Outline each blood parasite and name the species.
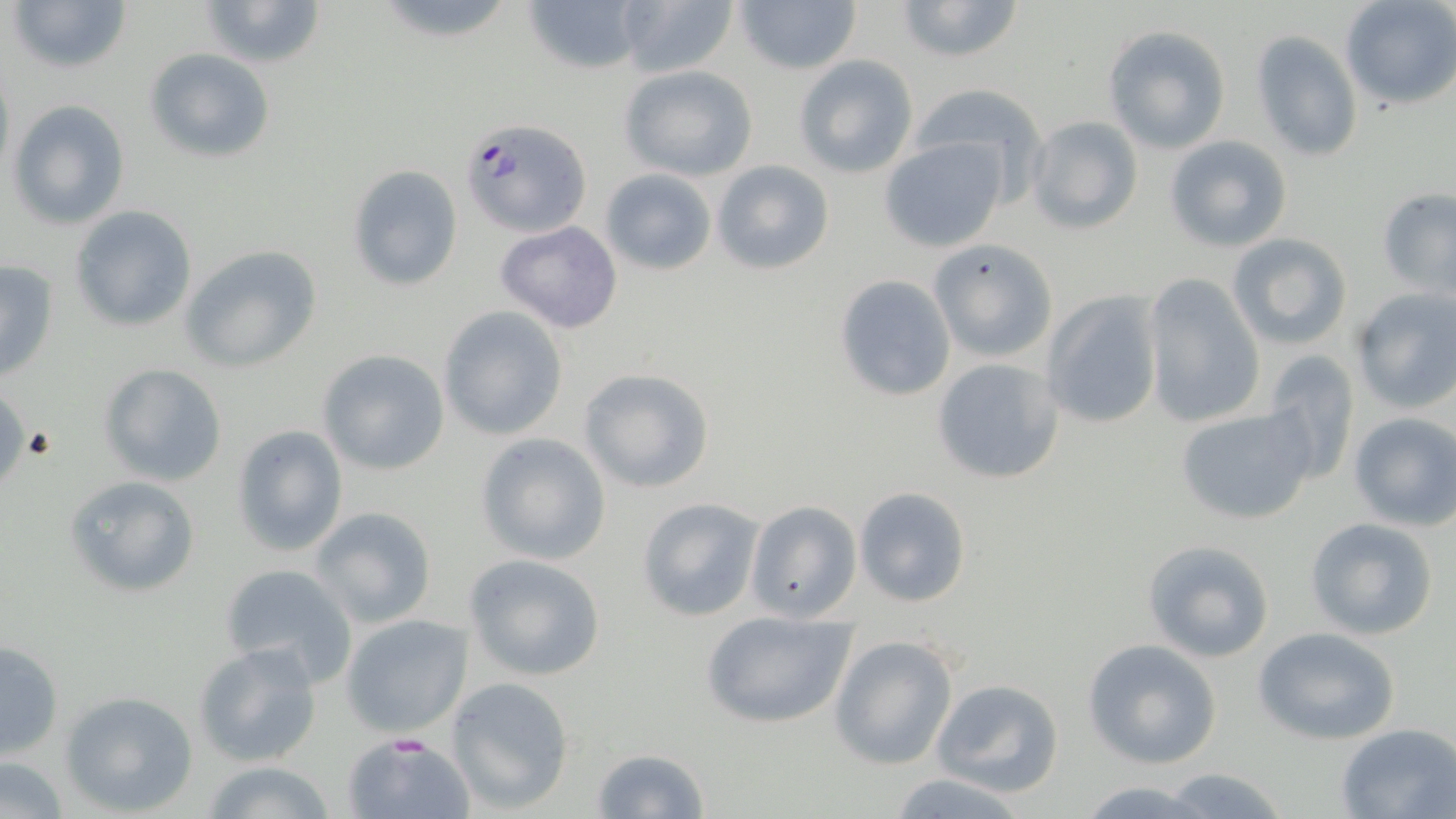

Approximate bounding boxes as (x1,y1)-(x2,y2) corner pairs in pixels.
Plasmodium falciparum-infected red blood cells: (460,120)-(590,238).
No Plasmodium ovale, Plasmodium malariae, Plasmodium vivax, Babesia divergens, or Trypanosoma brucei observed.

{
  "slide_level_diagnosis": "Plasmodium falciparum",
  "uninfected_red_blood_cell_locations": "approximate bounding boxes as (x1,y1)-(x2,y2) corner pairs in pixels: (7,0)-(132,72), (198,0)-(326,70), (518,0)-(651,74), (732,0)-(863,73), (894,0)-(1024,64), (1339,0)-(1456,109), (612,2)-(737,77), (1103,26)-(1230,152), (1249,31)-(1364,162), (1123,42)-(1258,210), (144,49)-(274,164), (793,54)-(919,178), (619,64)-(758,181), (909,83)-(1048,202), (6,100)-(131,229), (1027,116)-(1143,236), (1164,134)-(1293,252), (879,139)-(1008,252), (712,159)-(835,275), (347,164)-(463,291), (601,168)-(717,275), (1377,187)-(1456,296), (70,205)-(197,332), (495,221)-(623,334), (1228,233)-(1353,351), (929,239)-(1057,362), (179,245)-(322,372), (1,257)-(59,383), (1141,272)-(1266,429), (834,273)-(957,401), (1349,286)-(1456,414), (1040,289)-(1165,430), (437,305)-(568,441), (317,348)-(450,475), (1259,353)-(1361,487), (932,356)-(1066,485), (98,363)-(227,487), (577,368)-(713,495), (1174,404)-(1316,526), (1347,412)-(1456,530), (230,425)-(349,557), (475,433)-(611,566), (65,474)-(199,597), (852,485)-(973,608), (636,497)-(764,621), (744,499)-(862,623), (309,506)-(437,629), (1304,518)-(1438,641), (1142,540)-(1274,663), (464,554)-(605,681), (219,562)-(359,686), (699,610)-(858,730), (341,613)-(473,737), (1254,627)-(1400,744), (829,634)-(959,770), (1083,638)-(1223,769), (0,640)-(64,761), (192,641)-(323,768), (446,676)-(574,813), (931,677)-(1065,799), (62,690)-(197,815), (1336,724)-(1456,819), (342,733)-(474,819), (589,748)-(709,818), (0,752)-(70,819), (201,761)-(337,819), (1156,767)-(1292,819), (889,771)-(1035,818), (1072,781)-(1221,816)",
  "image_size": "1456×819 pixels",
  "magnification": "1000x",
  "preparation": "thin blood smear",
  "modality": "optical microscopy",
  "field_of_view": "single",
  "stain": "May-Grünwald-Giemsa"
}